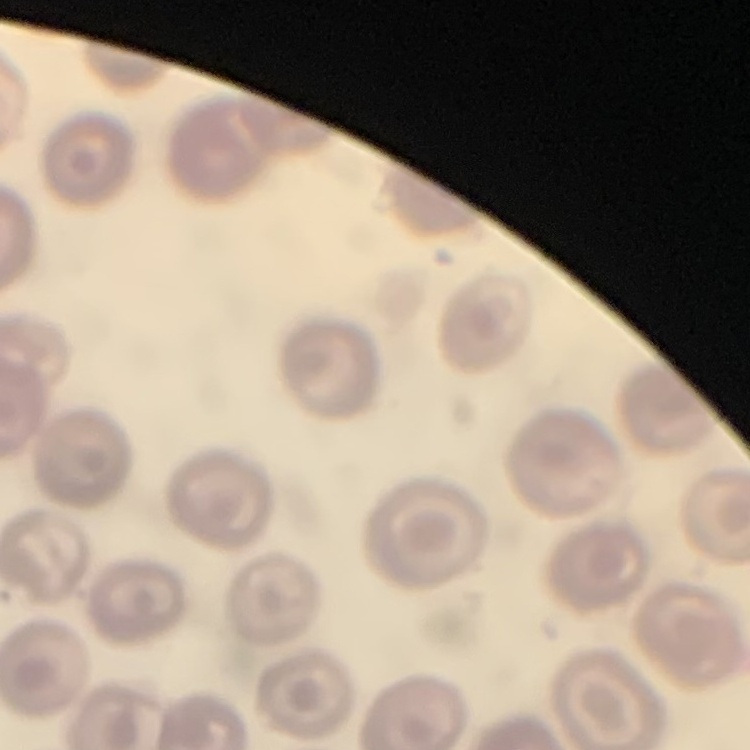 The red blood cells show no rouleaux formation. Field's or Giemsa stain. Thin peripheral smear. Square crop of a larger photomicrograph.